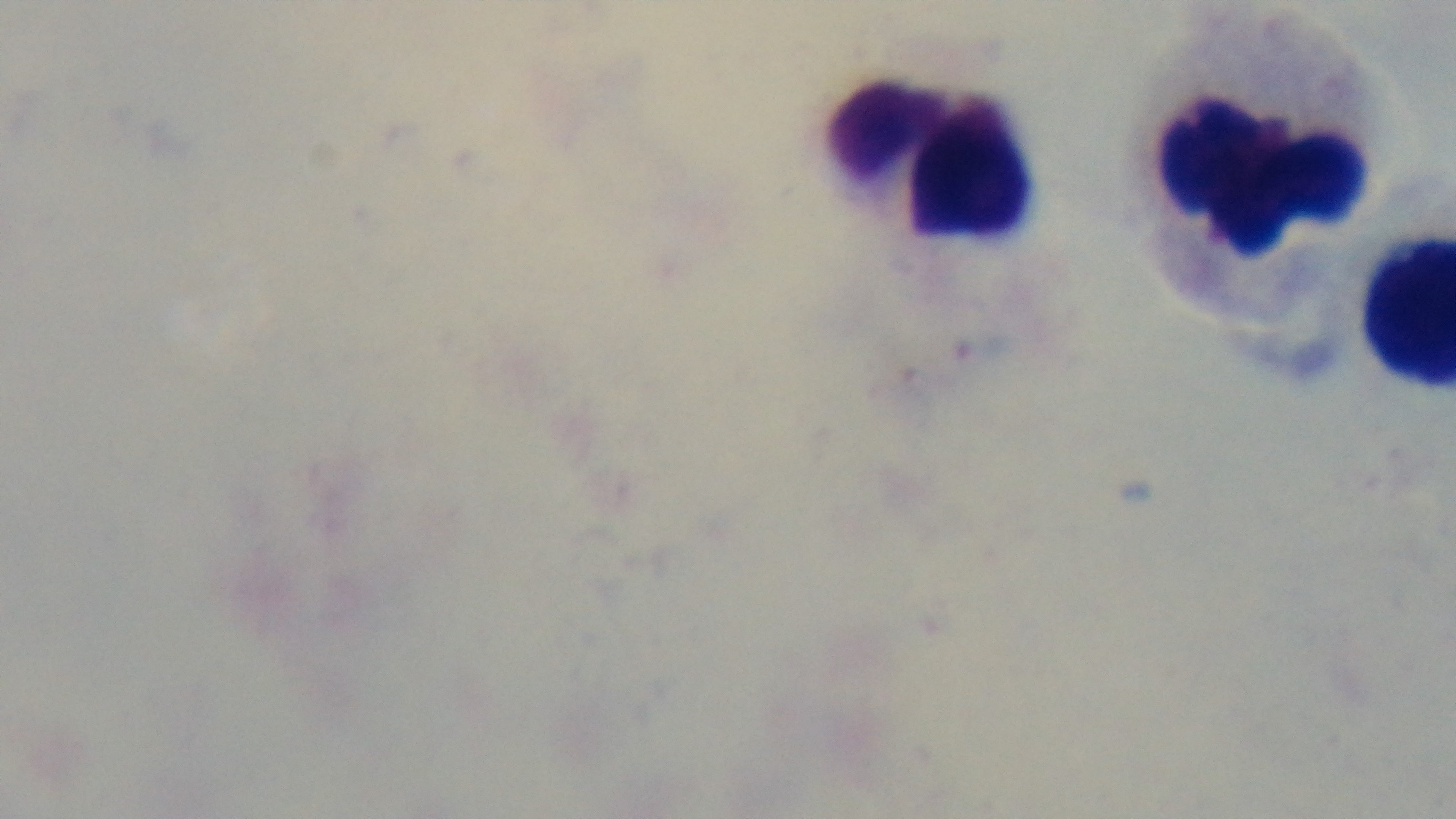

Summary:
  - Capture: mounted 4K digital camera
  - Objective: 100x oil immersion
  - Malaria status: uninfected
  - Field of view: single
  - Stain: Giemsa
  - Preparation: thick
  - Modality: light microscopy